Name the parasite shown.
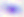
This is Toxoplasma gondii.

Photomicrograph. Captured at 400x magnification.